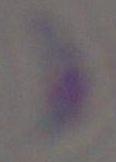

1000x magnification. Photomicrograph. Toxoplasma gondii is shown.